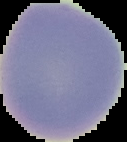

image type = cell region segmented out of the field of view; surrounding area masked to black
preparation = thin blood smear
image size = 127×142 pixels
malaria status = uninfected